Classify this cell by malaria status.
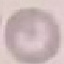
Uninfected.

Summary:
  - Capture: smartphone camera at the microscope eyepiece
  - Image type: cell patch, automatically extracted from a larger field of view and resized to 64 × 64 pixels
  - Preparation: thin blood smear
  - Stain: Giemsa